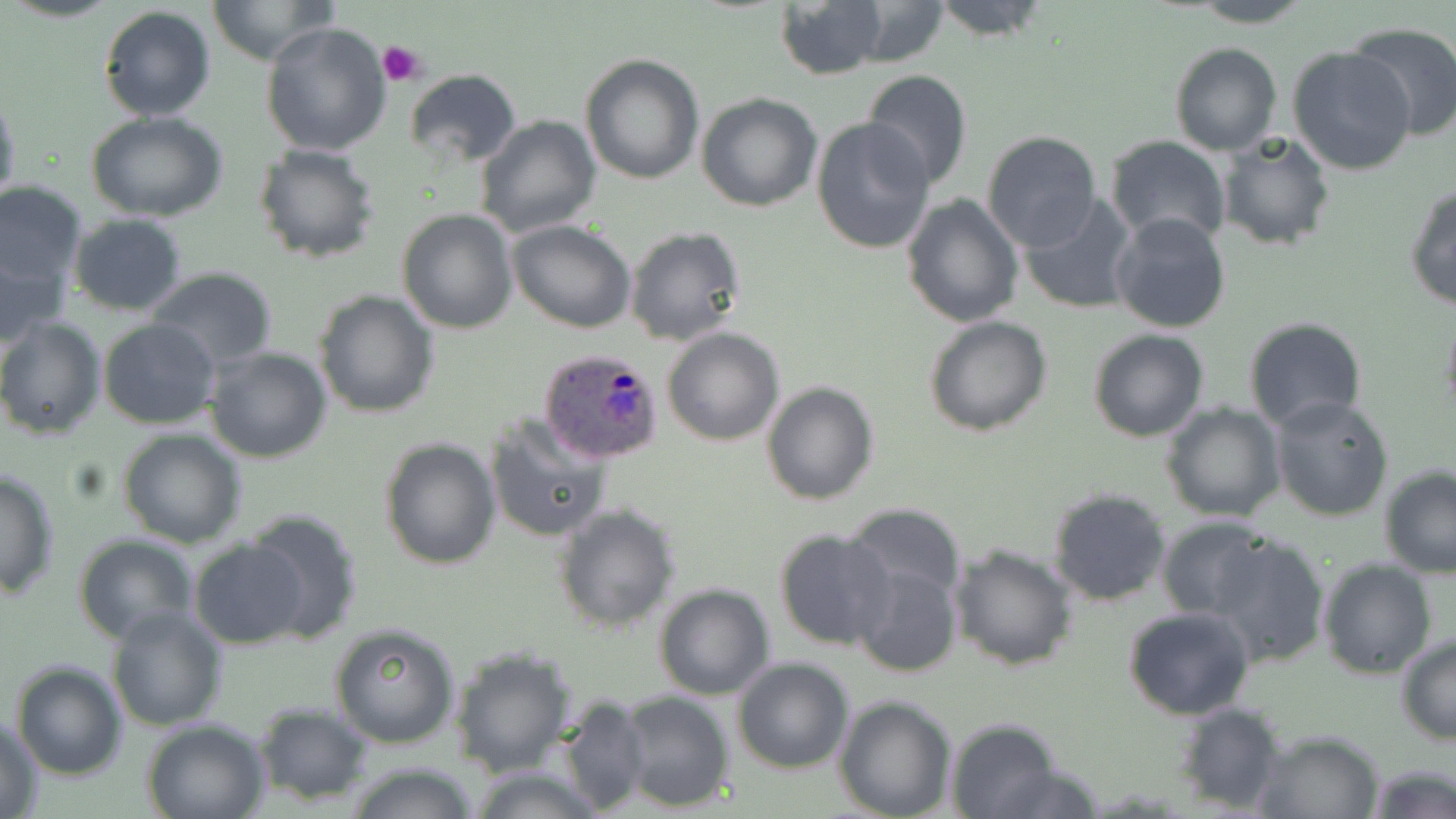
{
  "slide_level_diagnosis": "Plasmodium ovale",
  "uninfected_red_blood_cell_locations": "approximate bounding boxes as named x1/y1/x2/y2 corners in pixels: (x1=207, y1=0, x2=336, y2=66), (x1=775, y1=0, x2=888, y2=81), (x1=926, y1=0, x2=1052, y2=42), (x1=842, y1=1, x2=951, y2=67), (x1=1186, y1=1, x2=1316, y2=28), (x1=98, y1=6, x2=217, y2=122), (x1=260, y1=20, x2=393, y2=157), (x1=1346, y1=21, x2=1456, y2=142), (x1=1168, y1=41, x2=1281, y2=157), (x1=1288, y1=47, x2=1418, y2=177), (x1=580, y1=53, x2=705, y2=185), (x1=403, y1=69, x2=522, y2=166), (x1=862, y1=69, x2=972, y2=190), (x1=0, y1=89, x2=21, y2=216), (x1=696, y1=92, x2=821, y2=211), (x1=88, y1=112, x2=228, y2=222), (x1=476, y1=115, x2=602, y2=239), (x1=810, y1=115, x2=936, y2=255), (x1=1218, y1=129, x2=1335, y2=253), (x1=981, y1=130, x2=1102, y2=251), (x1=1107, y1=137, x2=1232, y2=247), (x1=252, y1=143, x2=381, y2=263), (x1=0, y1=180, x2=87, y2=291), (x1=1404, y1=181, x2=1456, y2=311), (x1=1019, y1=192, x2=1140, y2=314), (x1=901, y1=194, x2=1024, y2=328), (x1=397, y1=208, x2=520, y2=332), (x1=66, y1=213, x2=188, y2=315), (x1=1112, y1=213, x2=1230, y2=334), (x1=508, y1=220, x2=637, y2=333), (x1=625, y1=226, x2=747, y2=347), (x1=1, y1=247, x2=68, y2=349), (x1=145, y1=268, x2=278, y2=371), (x1=313, y1=289, x2=439, y2=417), (x1=1439, y1=305, x2=1456, y2=428), (x1=238, y1=313, x2=431, y2=440), (x1=0, y1=316, x2=106, y2=440), (x1=923, y1=316, x2=1052, y2=437), (x1=97, y1=317, x2=220, y2=429), (x1=1242, y1=317, x2=1367, y2=432), (x1=662, y1=327, x2=784, y2=446), (x1=1087, y1=329, x2=1211, y2=442), (x1=205, y1=345, x2=332, y2=463), (x1=760, y1=382, x2=880, y2=506), (x1=1269, y1=393, x2=1397, y2=523), (x1=1160, y1=401, x2=1285, y2=521), (x1=484, y1=412, x2=611, y2=543), (x1=118, y1=428, x2=246, y2=548), (x1=380, y1=437, x2=501, y2=571), (x1=0, y1=466, x2=60, y2=599), (x1=1379, y1=466, x2=1456, y2=577), (x1=1048, y1=486, x2=1174, y2=607), (x1=554, y1=503, x2=679, y2=633), (x1=845, y1=504, x2=968, y2=603), (x1=242, y1=509, x2=361, y2=645), (x1=1156, y1=516, x2=1272, y2=621), (x1=773, y1=527, x2=895, y2=651), (x1=1206, y1=531, x2=1331, y2=668), (x1=72, y1=534, x2=198, y2=644), (x1=189, y1=537, x2=307, y2=650), (x1=947, y1=542, x2=1077, y2=670), (x1=1317, y1=558, x2=1437, y2=679), (x1=850, y1=562, x2=962, y2=680), (x1=652, y1=583, x2=777, y2=700), (x1=1122, y1=604, x2=1254, y2=720), (x1=106, y1=607, x2=229, y2=732), (x1=329, y1=622, x2=460, y2=748), (x1=1395, y1=636, x2=1455, y2=746), (x1=447, y1=647, x2=577, y2=776), (x1=733, y1=657, x2=854, y2=772), (x1=10, y1=659, x2=127, y2=780), (x1=617, y1=691, x2=734, y2=812), (x1=833, y1=694, x2=959, y2=819), (x1=557, y1=696, x2=651, y2=816), (x1=1173, y1=701, x2=1288, y2=814), (x1=253, y1=705, x2=373, y2=803), (x1=2, y1=714, x2=44, y2=817), (x1=140, y1=718, x2=270, y2=819), (x1=943, y1=718, x2=1062, y2=819), (x1=1253, y1=729, x2=1386, y2=818), (x1=344, y1=762, x2=482, y2=819), (x1=1365, y1=764, x2=1455, y2=819), (x1=464, y1=767, x2=602, y2=819)",
  "modality": "optical microscopy",
  "preparation": "thin blood smear",
  "magnification": "1000x",
  "platelet_locations": "approximate bounding boxes as named x1/y1/x2/y2 corners in pixels: (x1=377, y1=38, x2=428, y2=86)",
  "stain": "May-Grünwald-Giemsa",
  "field_of_view": "one of a larger specimen",
  "plasmodium_ovale_infected_red_blood_cell_locations": "approximate bounding boxes as named x1/y1/x2/y2 corners in pixels: (x1=539, y1=347, x2=663, y2=463)",
  "image_size": "1456×819 pixels"
}